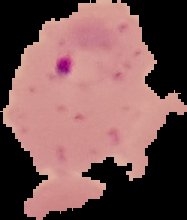 From a thin blood film. Malaria status: parasitized. Cell region segmented out of the field of view; the surrounding area is masked to black. Image is 187×220 pixels.